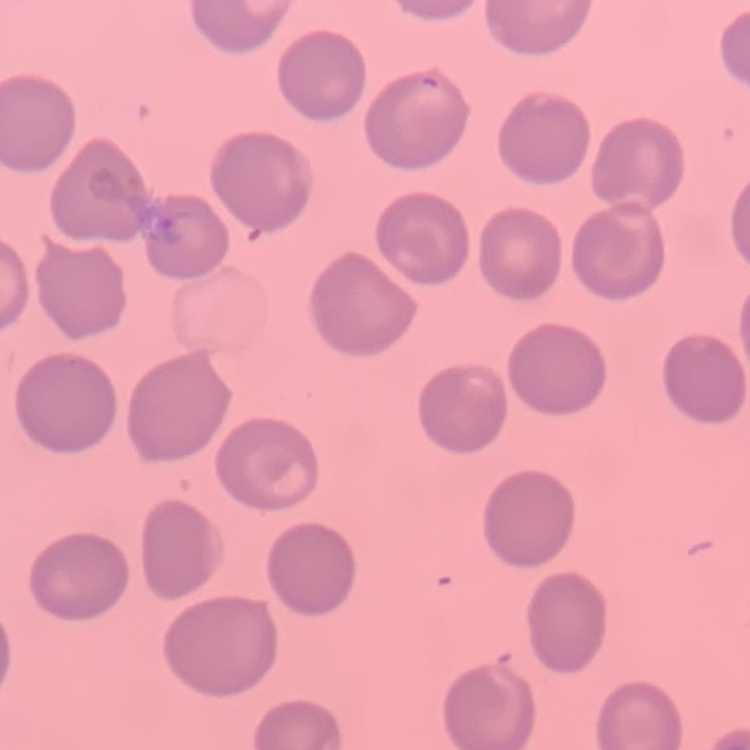

Summary:
  - Red blood cell morphology: no rouleaux formation
  - Image type: square crop of a larger photomicrograph
  - Preparation: thin blood film
  - Stain: Field's or Giemsa